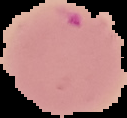

image size = 127×118 pixels
image type = segmented cell region with the area outside set to black
result = malaria parasites detected
preparation = thin blood film